Classify this cell by malaria status.
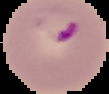

It is parasitized.

Image is 109×94 pixels. The area outside the segmented cell region is set to black. From a thin blood film.